Name the parasite shown.
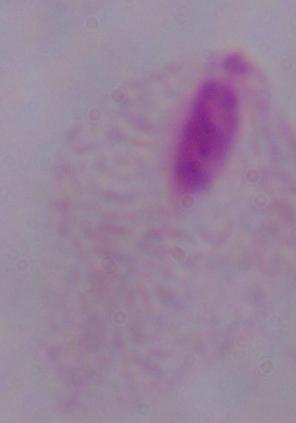

This is a trichomonad.

Photomicrograph. 1000x magnification.